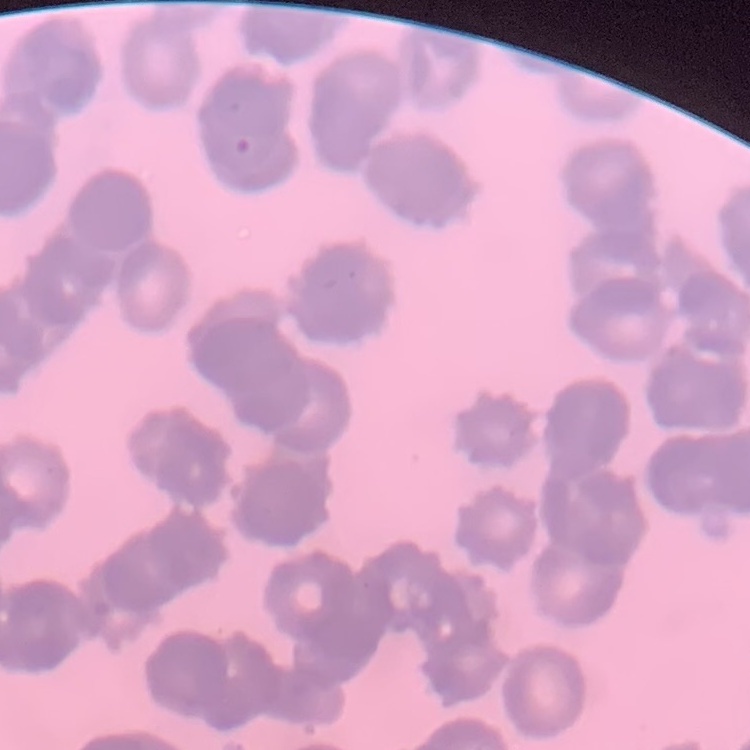
Summary:
  - Red blood cell morphology: rouleaux formation
  - Stain: Field's or Giemsa
  - Preparation: thin peripheral smear
  - Image type: square crop of a larger photomicrograph